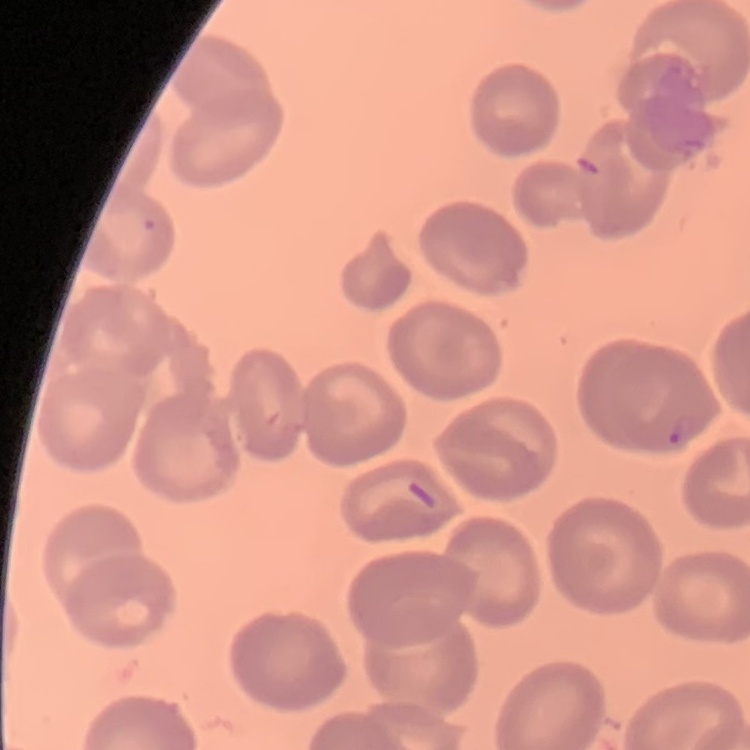
The red blood cells exhibit no rouleaux formation. Field's or Giemsa stain. Square crop of a larger photomicrograph. Thin peripheral smear.